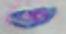

identification: Toxoplasma gondii
magnification: 1000x
modality: micrograph